Locate and identify every blood parasite.
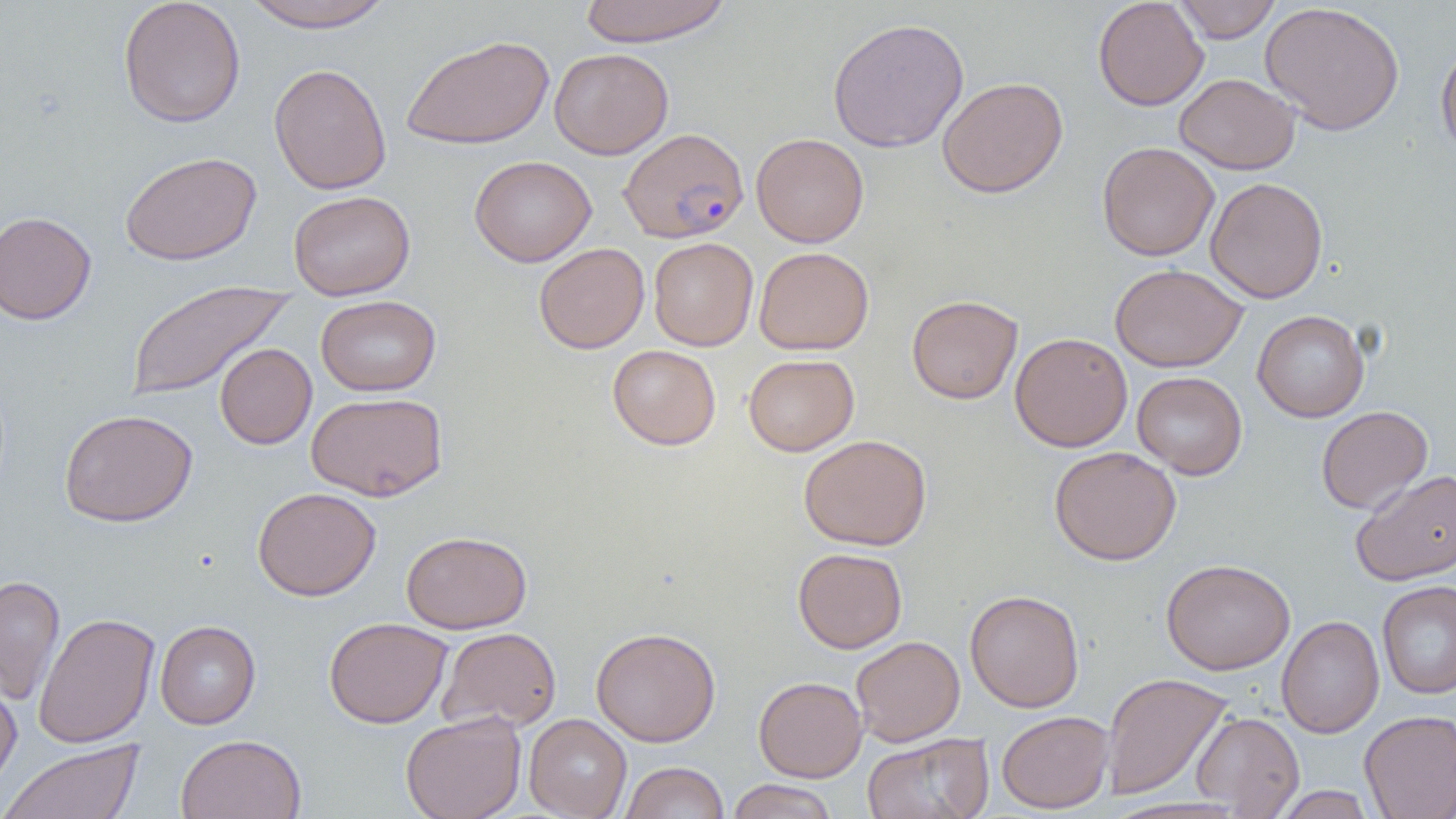

Approximate bounding boxes as (x1,y1)-(x2,y2) corner pairs in pixels.
Plasmodium falciparum-infected red blood cells: (619,126)-(749,242).
No Plasmodium ovale, Plasmodium malariae, Plasmodium vivax, Babesia divergens, or Trypanosoma brucei observed.

Uninfected red blood cell locations: (118,0)-(246,128), (241,0)-(396,33), (578,0)-(731,46), (1093,0)-(1209,111), (1173,0)-(1281,43), (1260,2)-(1405,136), (827,17)-(969,153), (401,34)-(554,150), (1436,42)-(1456,163), (549,47)-(674,159), (268,62)-(392,195), (1174,73)-(1300,174), (937,77)-(1068,198), (751,133)-(869,248), (1097,142)-(1219,261), (120,151)-(261,265), (469,155)-(596,267), (1205,177)-(1328,304), (288,190)-(415,300), (0,211)-(97,325), (648,237)-(758,351), (533,243)-(650,354), (754,247)-(874,355), (1109,263)-(1248,373), (126,279)-(295,401), (906,294)-(1023,404), (315,295)-(441,396), (1252,310)-(1369,422), (1010,332)-(1133,452), (214,343)-(317,449), (607,345)-(721,450), (743,353)-(859,456), (1132,371)-(1247,480), (306,392)-(447,501), (1316,405)-(1433,514), (59,408)-(198,527), (798,434)-(932,551), (1049,446)-(1181,566), (1351,469)-(1456,586), (252,487)-(381,601), (401,530)-(532,634), (793,547)-(907,653), (1161,558)-(1295,675), (0,574)-(66,706), (1377,580)-(1456,700), (965,589)-(1084,712), (33,611)-(160,749), (1276,615)-(1385,738), (324,617)-(452,728), (155,620)-(261,729), (590,626)-(721,746), (436,627)-(562,733), (851,635)-(965,746), (1101,672)-(1233,801), (754,676)-(867,782), (0,677)-(21,796), (1359,709)-(1456,818), (400,710)-(526,819), (996,710)-(1114,814), (1191,711)-(1304,817), (524,714)-(631,818), (862,732)-(994,819), (175,733)-(306,819), (1,739)-(145,819), (620,762)-(729,819), (726,779)-(839,819), (1273,786)-(1377,818). Slide-level diagnosis: Plasmodium falciparum. Single field of view. Light microscopy. Captured at 1000x magnification. Thin blood film. Image is 1456×819 pixels.